Find each WBC.
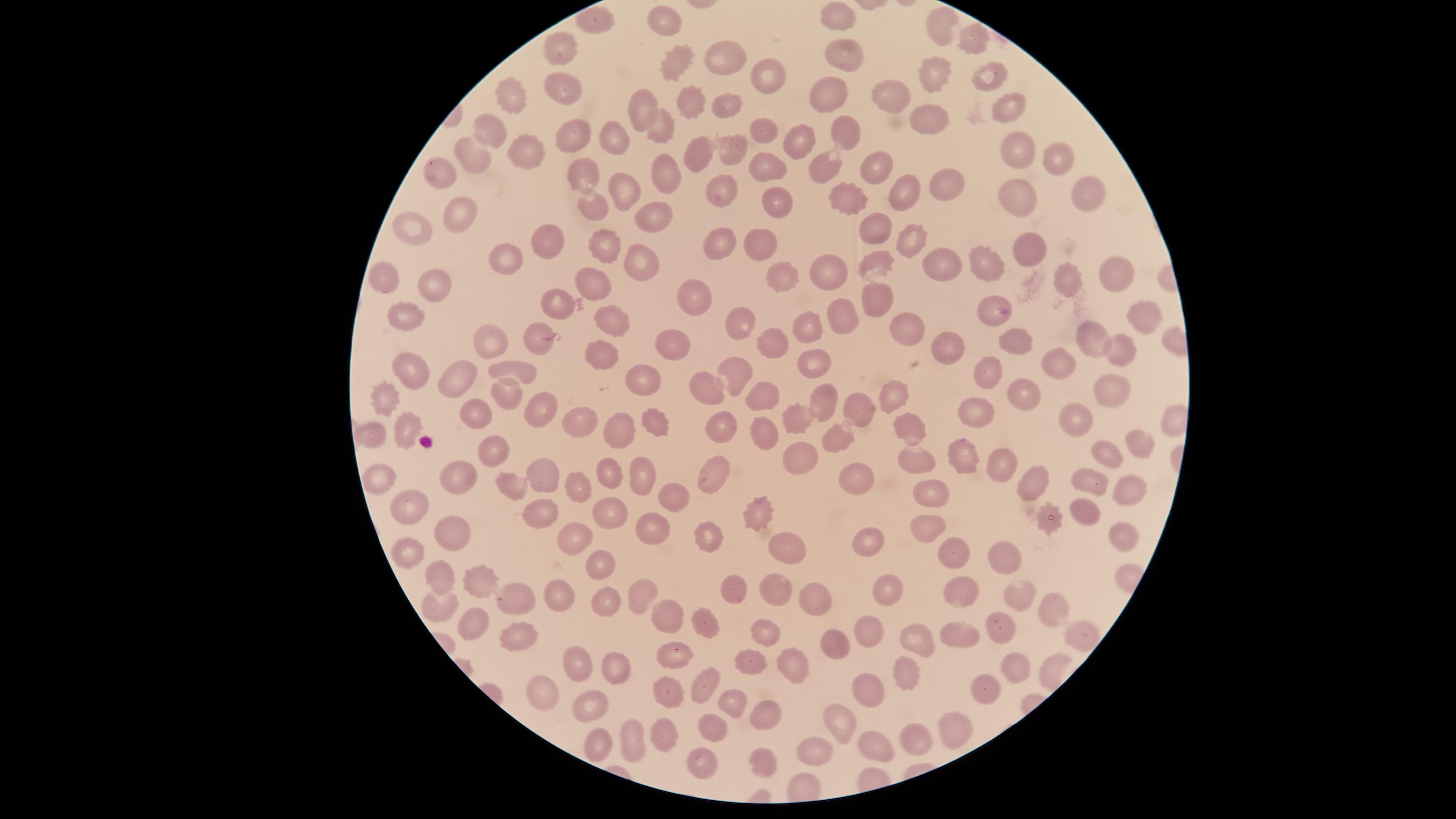
No WBCs identified.

Approximate marker points as [x, y] in pixels.
Summary:
  - Uninfected RBCs: [840, 14], [665, 18], [592, 21], [942, 27], [968, 45], [557, 46], [844, 55], [719, 56], [672, 65], [991, 72], [764, 77], [929, 79], [566, 91], [891, 92], [507, 100], [826, 101], [691, 103], [724, 107], [1004, 107], [639, 110], [930, 115], [659, 126], [767, 128], [492, 131], [843, 133], [568, 134], [616, 139], [799, 147], [1016, 149], [736, 151], [530, 153], [696, 153], [1053, 155], [473, 157], [824, 168], [770, 169], [872, 169], [578, 172], [439, 173], [660, 173], [945, 189], [624, 191], [1084, 192], [722, 193], [901, 194], [781, 199], [850, 199], [1014, 199], [588, 207], [459, 214], [650, 217], [416, 227], [876, 227], [763, 238], [720, 241], [909, 242], [550, 243], [604, 245], [1030, 253], [502, 254], [986, 261], [639, 263], [876, 264], [940, 266], [837, 271], [1122, 273], [782, 275], [388, 278], [588, 280], [1069, 284], [429, 286], [700, 294], [872, 302], [546, 303], [992, 310], [406, 312], [1143, 316], [734, 320], [840, 321], [609, 322], [803, 325], [900, 331], [1084, 333], [538, 336], [1013, 338], [675, 341], [767, 341], [494, 343], [1109, 349], [945, 351], [602, 355], [815, 365], [1056, 367], [512, 369], [734, 371], [989, 372], [410, 373], [463, 377], [644, 379], [1110, 390], [505, 391], [704, 392], [762, 394], [1024, 395], [895, 396], [821, 398], [386, 401], [545, 410], [855, 411], [799, 417], [477, 418], [981, 419], [653, 420], [577, 421], [1083, 425], [721, 427], [401, 428], [621, 429], [765, 432], [911, 433], [371, 434], [831, 435], [1144, 443], [496, 447], [961, 454], [1109, 455], [797, 456], [913, 460], [993, 462], [851, 468], [609, 471], [546, 472], [712, 476], [642, 478], [1093, 479], [381, 481], [463, 482], [1032, 483], [1129, 485], [509, 486], [577, 486], [930, 493], [671, 494], [411, 505], [1091, 512], [604, 513], [539, 515], [763, 515], [1048, 520], [649, 526], [926, 528], [451, 533], [1116, 533], [569, 537], [712, 537], [869, 539], [785, 548], [408, 552], [949, 556], [998, 556], [598, 566], [443, 576], [472, 580], [771, 587], [884, 592], [968, 592], [1013, 592], [643, 593], [737, 594], [609, 595], [558, 596], [814, 598], [527, 601], [443, 606], [1050, 607], [662, 616], [868, 623], [468, 624], [701, 624], [1002, 628], [958, 631], [767, 633], [1079, 633], [520, 637], [916, 639], [840, 646], [671, 653], [572, 664], [750, 664], [791, 664], [1020, 668], [619, 669], [905, 673], [703, 686], [873, 690], [667, 693], [987, 693], [539, 694], [596, 703], [735, 704], [763, 714], [836, 717], [714, 728], [911, 728], [656, 731], [954, 732], [629, 737], [592, 741], [876, 745], [817, 750], [759, 761], [703, 763]
  - Stain: Giemsa
  - Presence: no malaria parasites detected
  - Capture: smartphone photograph through the microscope eyepiece
  - Visible region: circular
  - Field of view: single
  - Image size: 1456×819 pixels
  - Preparation: thin blood film